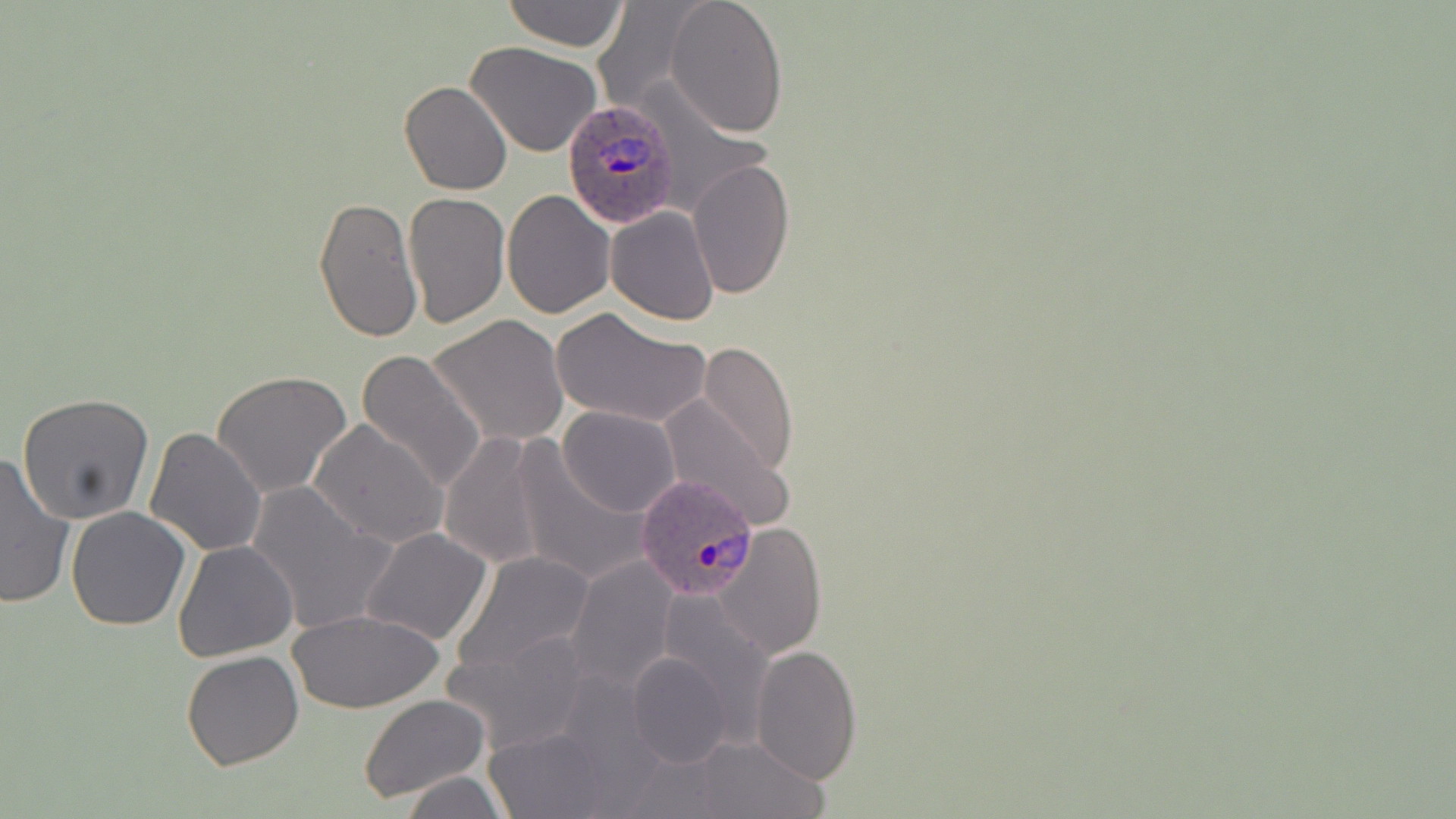

slide-level diagnosis = Plasmodium ovale
field of view = single
magnification = 1000x
image size = 1456×819 pixels
stain = May-Grünwald-Giemsa
preparation = thin blood film
Plasmodium ovale-infected red blood cell locations = approximate bounding boxes as (x1, y1, x2, y2) in pixels: (561, 99, 681, 226), (634, 476, 762, 606)
modality = optical microscopy
uninfected red blood cell locations = approximate bounding boxes as (x1, y1, x2, y2) in pixels: (501, 0, 630, 50), (665, 0, 789, 138), (466, 41, 601, 157), (399, 80, 513, 196), (686, 158, 794, 301), (501, 189, 614, 318), (404, 191, 509, 328), (313, 194, 423, 344), (605, 206, 720, 326), (551, 306, 711, 430), (428, 315, 569, 446), (697, 342, 798, 477), (356, 349, 488, 495), (212, 370, 352, 498), (17, 392, 155, 524), (659, 394, 795, 529), (556, 406, 681, 517), (308, 420, 447, 549), (146, 427, 266, 557), (436, 434, 556, 571), (509, 445, 647, 587), (0, 448, 77, 609), (246, 482, 396, 635), (65, 506, 192, 631), (716, 522, 826, 659), (359, 527, 494, 645), (172, 540, 298, 663), (452, 550, 597, 679), (566, 556, 680, 690), (288, 608, 446, 712), (444, 629, 594, 753), (750, 644, 862, 784), (180, 650, 305, 770), (626, 651, 733, 768), (357, 693, 490, 804), (485, 724, 616, 818), (685, 734, 827, 818), (400, 772, 507, 818)